Assess the morphology of the red blood cells.
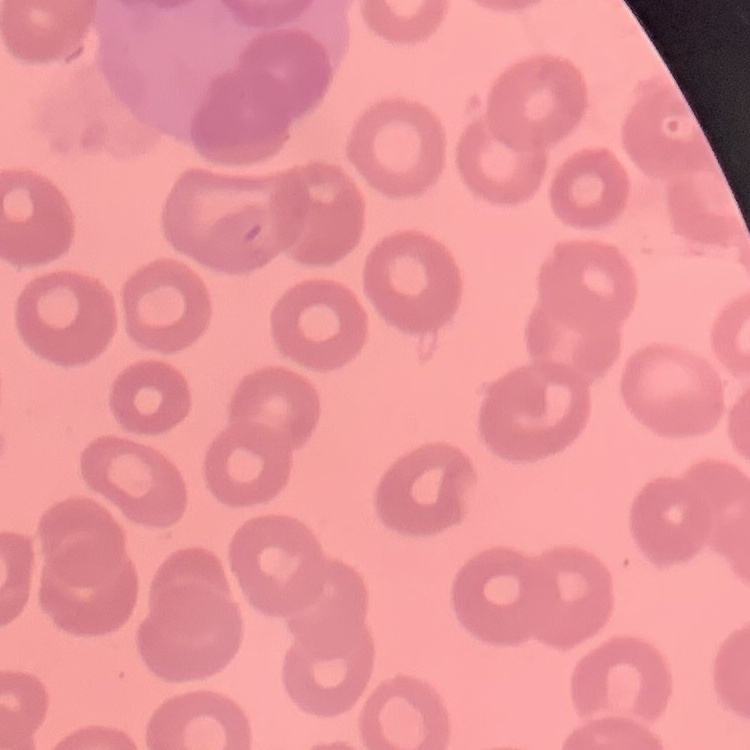
No rouleaux formation.

{
  "image_type": "one tile cut from a larger photomicrograph",
  "stain": "Field's or Giemsa",
  "preparation": "thin blood film"
}